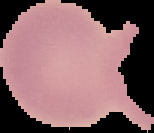
preparation = thin blood smear
result = no malaria parasites seen
image type = segmented cell region on a black background
image size = 154×133 pixels